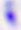

Micrograph. Toxoplasma gondii is seen. 400x magnification.